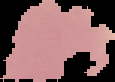

image type = segmented cell region on a black background
malaria status = uninfected
image size = 115×82 pixels
preparation = thin blood film